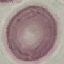
malaria status = uninfected
capture = smartphone through the microscope eyepiece
image type = automatically extracted cell patch, resized to 64 × 64 pixels
stain = Giemsa
preparation = thin blood film